Point out each malaria parasite.
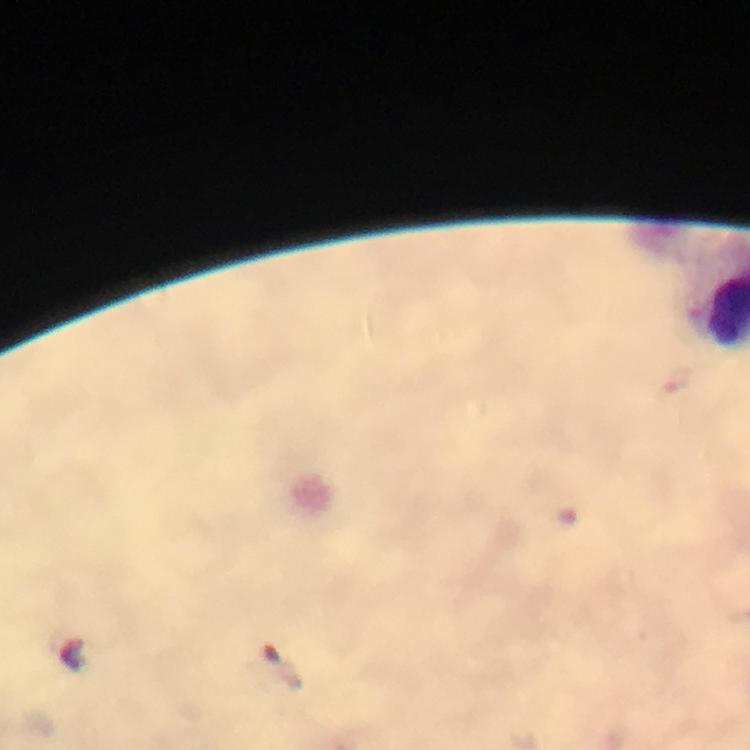
Approximate centers as (x, y) in pixels.
Malaria parasites: (284, 671).

immersion oil = applied
context = from a malaria diagnostic workup
cropped from = a single field of view
magnification = 100x
capture = smartphone mounted on the microscope
preparation = thick smear
image size = 750×750 pixels
stain = Giemsa